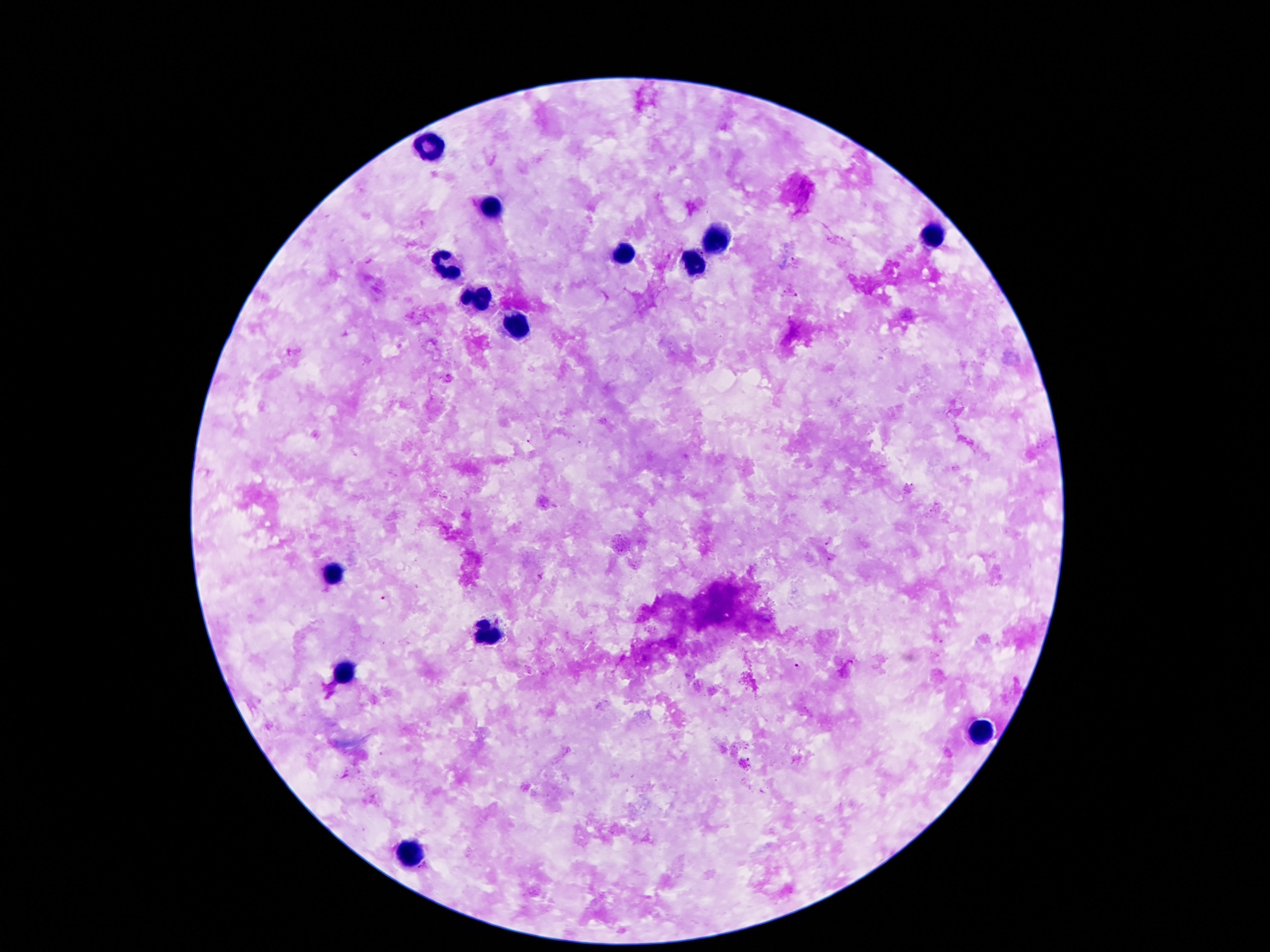

{
  "magnification": "100x",
  "image_size": "1270×952 pixels",
  "field_of_view": "one from this slide",
  "patient_malaria_status": "uninfected",
  "capture": "smartphone camera through the microscope eyepiece",
  "preparation": "thick blood film",
  "leukocyte_locations": "approximate centers as [x, y] in pixels: [433, 143], [492, 206], [931, 234], [711, 238], [624, 254], [693, 261], [446, 270], [471, 301], [515, 327], [331, 574], [489, 637], [344, 671], [978, 731], [410, 853]",
  "stain": "Giemsa"
}